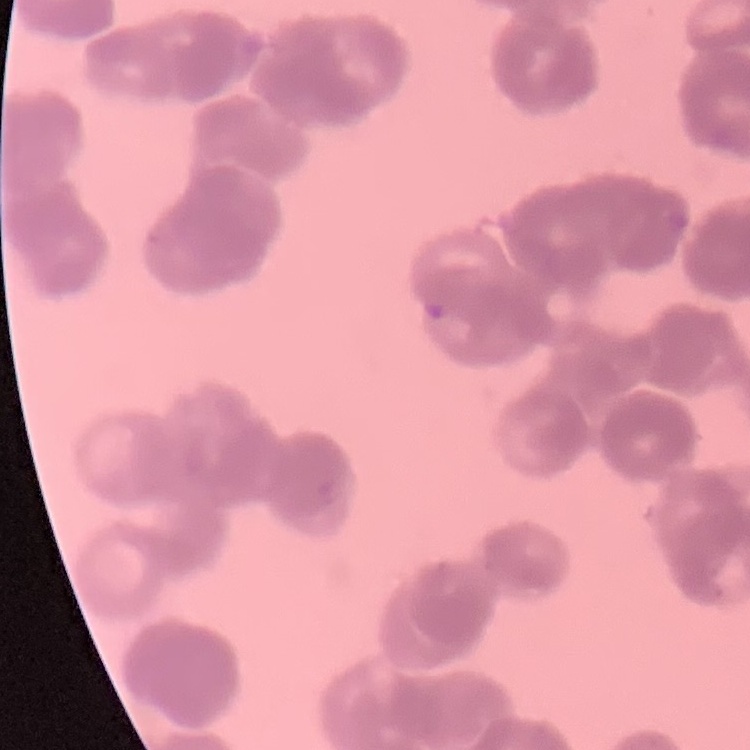
red blood cell morphology = rouleaux formation
stain = Field's or Giemsa
image type = square crop of a larger photomicrograph
preparation = thin blood film